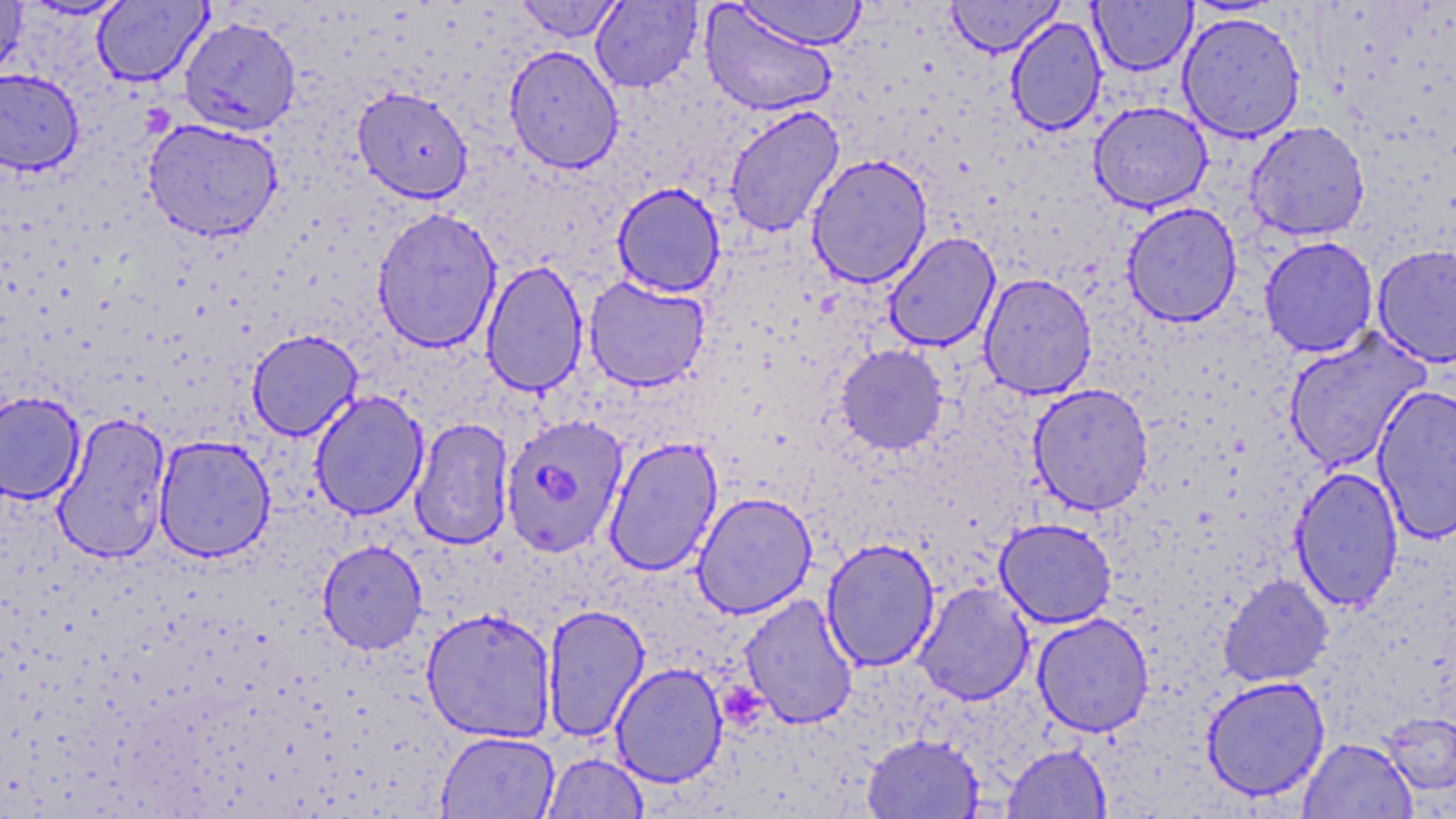
Approximate bounding boxes as named x1/y1/x2/y2 corners in pixels. Uninfected red blood cell locations: (x1=0, y1=0, x2=27, y2=81), (x1=21, y1=0, x2=133, y2=20), (x1=516, y1=0, x2=623, y2=43), (x1=736, y1=0, x2=867, y2=49), (x1=946, y1=0, x2=1063, y2=56), (x1=92, y1=1, x2=211, y2=86), (x1=590, y1=1, x2=702, y2=92), (x1=1089, y1=1, x2=1197, y2=75), (x1=699, y1=4, x2=838, y2=117), (x1=1177, y1=11, x2=1305, y2=143), (x1=178, y1=16, x2=302, y2=135), (x1=1005, y1=16, x2=1107, y2=136), (x1=503, y1=45, x2=624, y2=174), (x1=0, y1=68, x2=85, y2=175), (x1=352, y1=87, x2=473, y2=203), (x1=1088, y1=101, x2=1213, y2=213), (x1=724, y1=104, x2=846, y2=238), (x1=143, y1=119, x2=283, y2=242), (x1=1245, y1=121, x2=1370, y2=241), (x1=806, y1=153, x2=933, y2=289), (x1=612, y1=181, x2=726, y2=298), (x1=1121, y1=202, x2=1242, y2=327), (x1=371, y1=206, x2=503, y2=354), (x1=883, y1=232, x2=1000, y2=352), (x1=1259, y1=236, x2=1379, y2=357), (x1=1371, y1=243, x2=1456, y2=368), (x1=480, y1=259, x2=588, y2=397), (x1=978, y1=273, x2=1097, y2=399), (x1=583, y1=276, x2=710, y2=391), (x1=1283, y1=328, x2=1430, y2=474), (x1=246, y1=329, x2=363, y2=441), (x1=835, y1=344, x2=949, y2=454), (x1=1028, y1=384, x2=1153, y2=515), (x1=1372, y1=384, x2=1456, y2=545), (x1=309, y1=390, x2=430, y2=521), (x1=0, y1=392, x2=85, y2=504), (x1=52, y1=412, x2=171, y2=564), (x1=409, y1=417, x2=514, y2=550), (x1=153, y1=435, x2=276, y2=562), (x1=604, y1=435, x2=723, y2=577), (x1=1290, y1=465, x2=1404, y2=613), (x1=691, y1=492, x2=818, y2=618), (x1=994, y1=517, x2=1117, y2=628), (x1=821, y1=538, x2=940, y2=672), (x1=317, y1=540, x2=427, y2=654), (x1=1218, y1=573, x2=1334, y2=688), (x1=913, y1=581, x2=1035, y2=705), (x1=739, y1=593, x2=859, y2=729), (x1=542, y1=603, x2=650, y2=741), (x1=420, y1=608, x2=557, y2=743), (x1=1032, y1=613, x2=1154, y2=737), (x1=610, y1=663, x2=728, y2=787), (x1=1201, y1=675, x2=1330, y2=801), (x1=1380, y1=711, x2=1456, y2=796), (x1=436, y1=731, x2=559, y2=819), (x1=861, y1=733, x2=985, y2=818), (x1=1298, y1=738, x2=1418, y2=819), (x1=1002, y1=743, x2=1112, y2=818), (x1=542, y1=753, x2=648, y2=819). Platelet locations: (x1=724, y1=683, x2=767, y2=725). Plasmodium falciparum-infected red blood cell locations: (x1=500, y1=414, x2=630, y2=557). Slide-level diagnosis: Plasmodium falciparum. Thin blood smear. Optical microscopy. May-Grünwald-Giemsa-stained preparation. Single field of view. Captured at 1000x magnification. Image is 1456×819 pixels.